Assess the morphology of the erythrocytes.
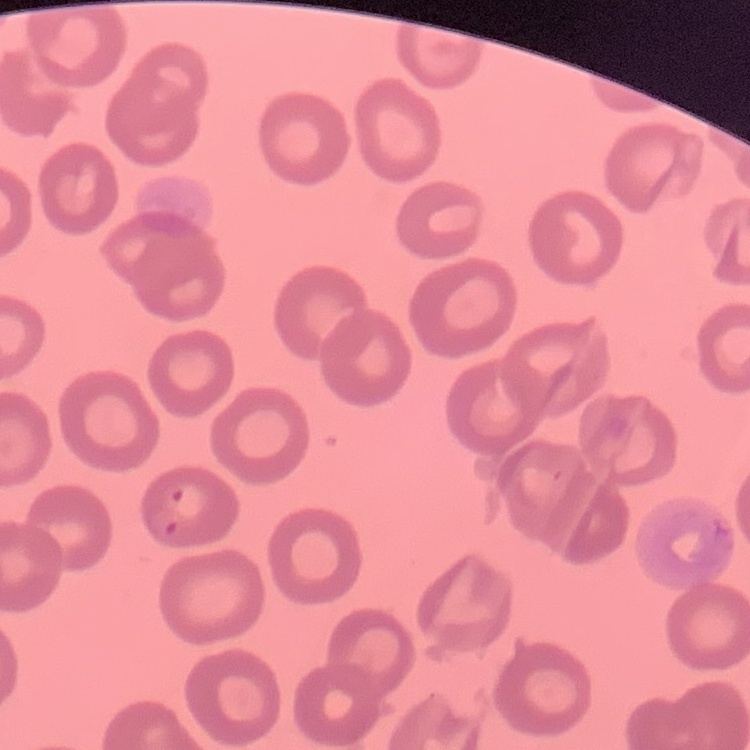
No rouleaux formation.

{
  "image_type": "one tile cut from a larger photomicrograph",
  "preparation": "thin blood smear",
  "stain": "Field's or Giemsa"
}